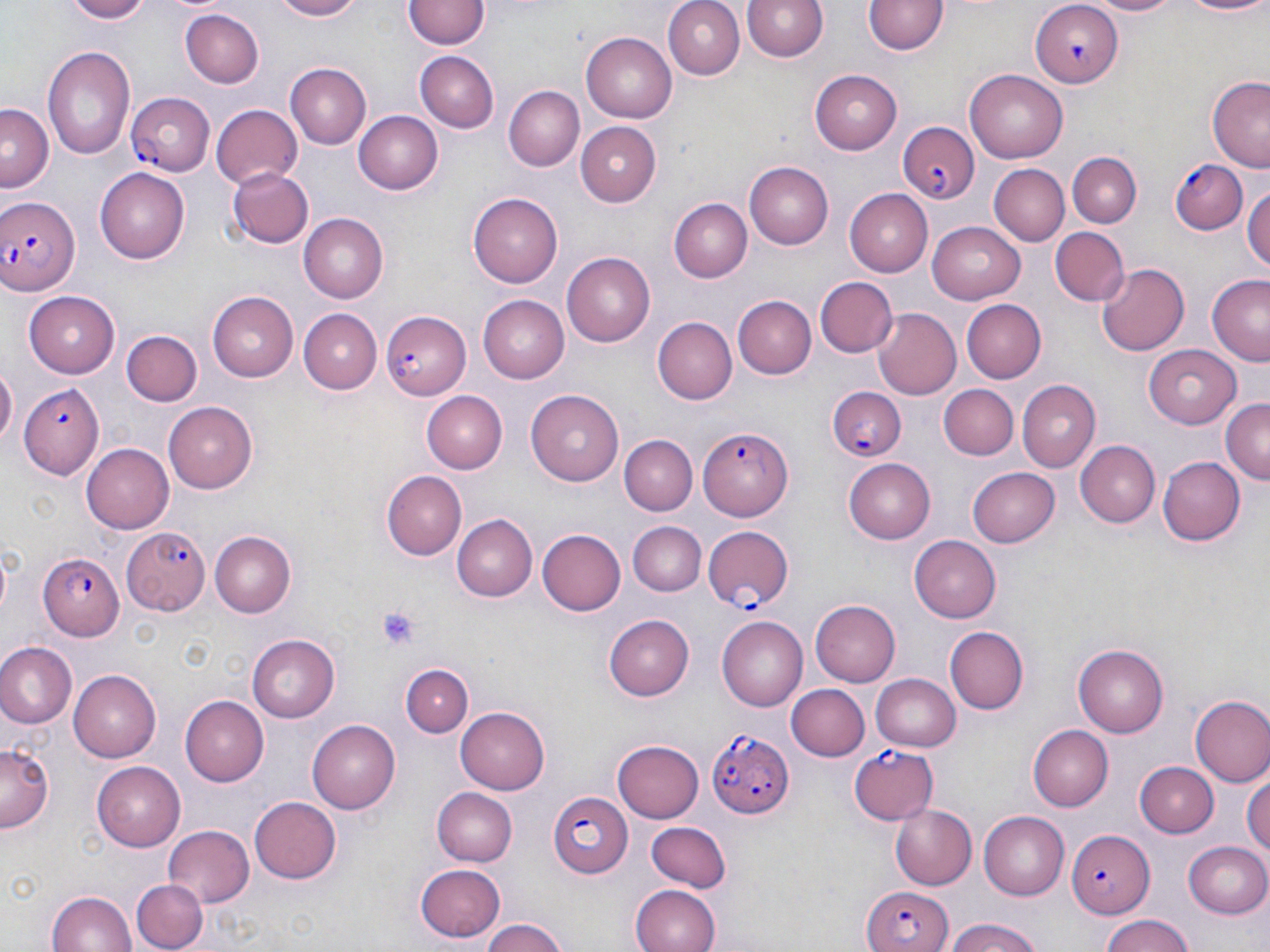
Approximate bounding boxes as named x1/y1/x2/y2 corners in pixels. Platelet locations: (x1=377, y1=605, x2=423, y2=651). Plasmodium falciparum-infected red blood cell locations: (x1=1029, y1=0, x2=1121, y2=86), (x1=127, y1=90, x2=214, y2=175), (x1=898, y1=122, x2=982, y2=204), (x1=1172, y1=161, x2=1248, y2=234), (x1=0, y1=192, x2=80, y2=295), (x1=378, y1=309, x2=471, y2=398), (x1=19, y1=382, x2=100, y2=476), (x1=825, y1=389, x2=907, y2=461), (x1=699, y1=426, x2=793, y2=521), (x1=122, y1=525, x2=210, y2=616), (x1=702, y1=525, x2=795, y2=610), (x1=40, y1=555, x2=123, y2=639), (x1=705, y1=727, x2=796, y2=821), (x1=848, y1=745, x2=939, y2=827), (x1=547, y1=790, x2=632, y2=875), (x1=1068, y1=828, x2=1155, y2=918), (x1=864, y1=883, x2=951, y2=952). Uninfected red blood cell locations: (x1=59, y1=0, x2=152, y2=23), (x1=267, y1=0, x2=365, y2=22), (x1=661, y1=0, x2=746, y2=80), (x1=741, y1=0, x2=830, y2=64), (x1=1082, y1=0, x2=1185, y2=17), (x1=1176, y1=0, x2=1270, y2=17), (x1=403, y1=1, x2=487, y2=51), (x1=866, y1=1, x2=947, y2=56), (x1=179, y1=9, x2=264, y2=88), (x1=581, y1=30, x2=677, y2=120), (x1=42, y1=45, x2=136, y2=162), (x1=415, y1=51, x2=498, y2=132), (x1=283, y1=63, x2=370, y2=149), (x1=967, y1=68, x2=1071, y2=163), (x1=809, y1=70, x2=903, y2=155), (x1=1208, y1=77, x2=1270, y2=169), (x1=504, y1=85, x2=585, y2=170), (x1=0, y1=105, x2=52, y2=191), (x1=212, y1=105, x2=301, y2=191), (x1=355, y1=110, x2=444, y2=195), (x1=574, y1=122, x2=660, y2=207), (x1=1068, y1=150, x2=1141, y2=225), (x1=743, y1=159, x2=833, y2=246), (x1=987, y1=164, x2=1068, y2=246), (x1=97, y1=167, x2=190, y2=262), (x1=228, y1=168, x2=313, y2=248), (x1=1243, y1=184, x2=1270, y2=277), (x1=846, y1=189, x2=936, y2=275), (x1=469, y1=192, x2=563, y2=285), (x1=669, y1=199, x2=750, y2=282), (x1=299, y1=213, x2=389, y2=302), (x1=928, y1=222, x2=1027, y2=301), (x1=1048, y1=227, x2=1130, y2=307), (x1=562, y1=251, x2=655, y2=347), (x1=1097, y1=261, x2=1192, y2=356), (x1=1204, y1=271, x2=1270, y2=362), (x1=815, y1=276, x2=896, y2=359), (x1=25, y1=290, x2=121, y2=375), (x1=208, y1=290, x2=301, y2=381), (x1=480, y1=294, x2=570, y2=383), (x1=733, y1=295, x2=814, y2=378), (x1=964, y1=299, x2=1046, y2=384), (x1=871, y1=307, x2=961, y2=399), (x1=299, y1=309, x2=382, y2=393), (x1=651, y1=317, x2=736, y2=405), (x1=123, y1=330, x2=202, y2=406), (x1=1145, y1=344, x2=1242, y2=426), (x1=0, y1=365, x2=16, y2=452), (x1=1016, y1=380, x2=1099, y2=472), (x1=937, y1=384, x2=1018, y2=460), (x1=423, y1=392, x2=507, y2=473), (x1=528, y1=392, x2=623, y2=484), (x1=1220, y1=398, x2=1270, y2=485), (x1=165, y1=401, x2=260, y2=493), (x1=619, y1=433, x2=697, y2=512), (x1=1074, y1=439, x2=1161, y2=528), (x1=81, y1=442, x2=173, y2=533), (x1=1157, y1=455, x2=1244, y2=547), (x1=845, y1=458, x2=940, y2=543), (x1=967, y1=467, x2=1059, y2=548), (x1=381, y1=472, x2=465, y2=559), (x1=453, y1=515, x2=536, y2=601), (x1=630, y1=521, x2=706, y2=597), (x1=535, y1=529, x2=623, y2=617), (x1=210, y1=531, x2=297, y2=616), (x1=912, y1=534, x2=1004, y2=622), (x1=812, y1=599, x2=903, y2=686), (x1=602, y1=612, x2=692, y2=702), (x1=717, y1=616, x2=810, y2=710), (x1=946, y1=627, x2=1030, y2=715), (x1=247, y1=634, x2=339, y2=722), (x1=0, y1=643, x2=75, y2=728), (x1=1073, y1=644, x2=1166, y2=736), (x1=401, y1=664, x2=473, y2=737), (x1=70, y1=669, x2=162, y2=761), (x1=869, y1=673, x2=961, y2=752), (x1=789, y1=685, x2=870, y2=760), (x1=181, y1=695, x2=268, y2=784), (x1=1190, y1=695, x2=1270, y2=787), (x1=455, y1=707, x2=550, y2=795), (x1=307, y1=719, x2=401, y2=814), (x1=1027, y1=724, x2=1114, y2=811), (x1=613, y1=737, x2=705, y2=823), (x1=1, y1=744, x2=53, y2=835), (x1=1137, y1=761, x2=1218, y2=837), (x1=91, y1=762, x2=183, y2=850), (x1=1243, y1=772, x2=1270, y2=864), (x1=432, y1=787, x2=517, y2=866), (x1=248, y1=796, x2=340, y2=884), (x1=888, y1=804, x2=978, y2=890), (x1=978, y1=811, x2=1068, y2=900), (x1=646, y1=822, x2=730, y2=893), (x1=162, y1=825, x2=254, y2=908), (x1=1185, y1=841, x2=1270, y2=917), (x1=415, y1=863, x2=506, y2=941), (x1=131, y1=879, x2=206, y2=951), (x1=629, y1=885, x2=721, y2=952), (x1=45, y1=889, x2=139, y2=952), (x1=1096, y1=915, x2=1202, y2=952), (x1=481, y1=918, x2=569, y2=952), (x1=941, y1=921, x2=1047, y2=952). Slide-level diagnosis: Plasmodium falciparum. One field of a larger specimen. Image is 1270×952 pixels. Thin blood smear. Optical microscopy. May-Grünwald-Giemsa stain. 1000x magnification.